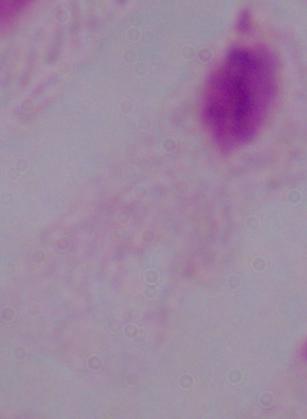
1000x magnification. A trichomonad is seen. Photomicrograph.